Point out each Plasmodium parasite.
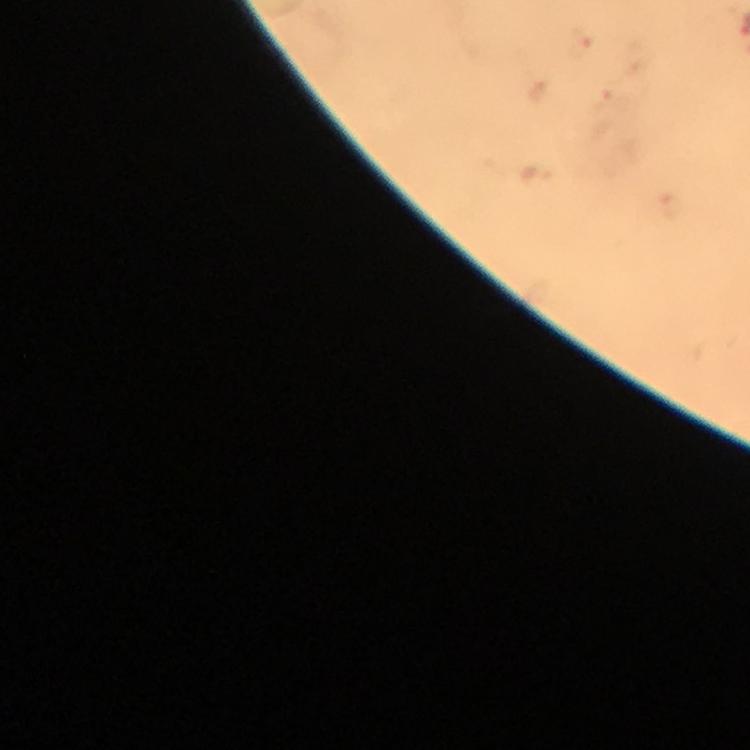

Approximate centers as (x, y) in pixels.
Plasmodium parasites: (579, 42).

Giemsa-stained preparation. At 100x magnification. From a diagnostic examination for malaria. Photographed through the microscope with a smartphone camera. Image is 750×750 pixels. Thick smear. Cropped region of a single field of view. Immersion oil applied.